Locate every blood parasite and identify its species.
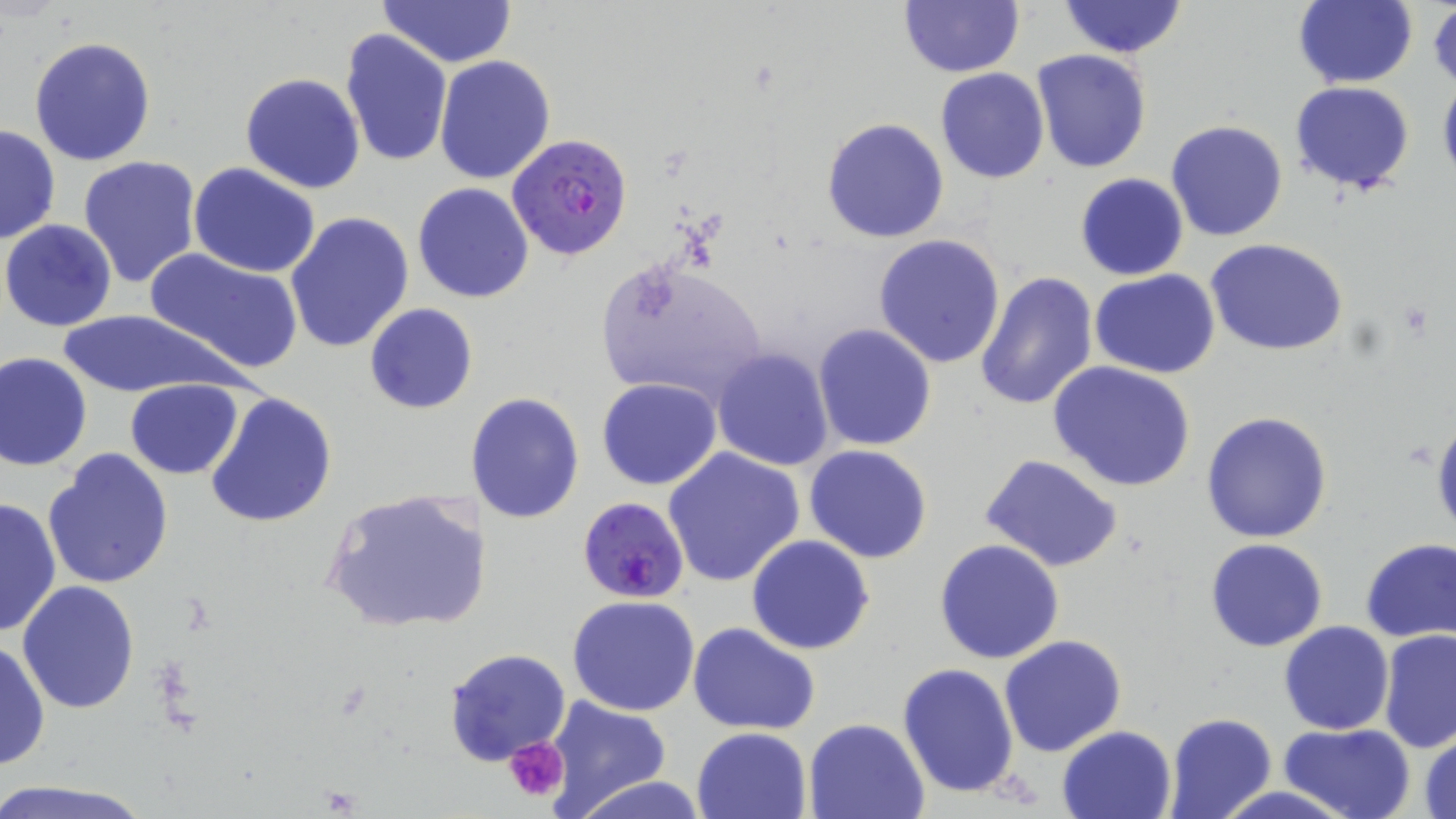

Approximate bounding boxes as (x1,y1)-(x2,y2) corner pairs in pixels.
Plasmodium falciparum-infected red blood cells: (507,133)-(634,261), (577,496)-(688,602).
No Plasmodium ovale, Plasmodium malariae, Plasmodium vivax, Babesia divergens, or Trypanosoma brucei observed.

Summary:
  - Uninfected red blood cell locations: (1294,0)-(1418,89), (378,1)-(516,68), (898,1)-(1023,77), (1056,1)-(1188,58), (1428,4)-(1456,91), (339,28)-(452,166), (29,36)-(157,167), (1031,49)-(1152,174), (434,55)-(556,184), (934,68)-(1049,184), (1437,72)-(1456,196), (240,73)-(365,193), (1289,81)-(1415,194), (821,117)-(949,243), (1165,120)-(1288,241), (0,122)-(61,246), (77,155)-(202,290), (189,162)-(322,278), (1074,173)-(1189,280), (413,182)-(534,304), (284,212)-(414,353), (1,219)-(119,332), (873,234)-(1006,370), (1206,238)-(1350,356), (143,247)-(304,374), (595,255)-(767,405), (1090,269)-(1221,380), (973,270)-(1101,413), (365,303)-(477,415), (57,308)-(236,399), (812,323)-(938,452), (711,347)-(834,471), (1,350)-(93,472), (1048,360)-(1196,492), (124,378)-(244,478), (597,378)-(723,490), (204,390)-(337,528), (472,391)-(586,525), (1201,410)-(1332,544), (1431,416)-(1456,541), (803,445)-(933,565), (662,447)-(807,588), (43,448)-(174,590), (978,454)-(1126,573), (321,488)-(486,635), (1,495)-(60,638), (746,535)-(875,656), (934,538)-(1065,664), (1206,539)-(1328,653), (1360,539)-(1456,644), (18,581)-(140,714), (568,596)-(700,716), (1279,621)-(1395,735), (687,623)-(821,734), (1377,630)-(1455,753), (1000,633)-(1127,757), (1,639)-(50,773), (443,648)-(573,767), (897,662)-(1020,798), (545,698)-(671,813), (1163,713)-(1277,819), (804,717)-(930,818), (1279,722)-(1415,819), (1057,725)-(1176,818), (692,727)-(811,818), (1417,729)-(1456,819), (568,775)-(713,819), (0,779)-(159,819)
  - Platelet locations: (505,737)-(569,801)
  - Slide-level diagnosis: Plasmodium falciparum
  - Stain: May-Grünwald-Giemsa
  - Modality: optical microscopy
  - Preparation: thin blood film
  - Field of view: single
  - Image size: 1456×819 pixels
  - Magnification: 1000x